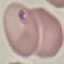

Summary:
  - Result: negative for malaria parasites
  - Image type: cell patch, automatically extracted from a larger field of view and resized to 64 × 64 pixels
  - Preparation: thin blood film
  - Capture: smartphone camera at the microscope eyepiece
  - Stain: Giemsa